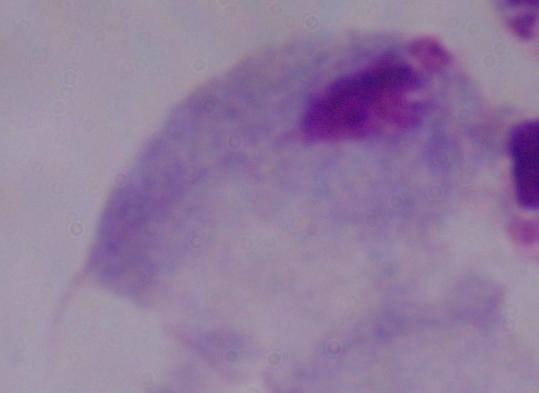

Summary:
  - Magnification: 1000x
  - Modality: micrograph
  - Identification: trichomonad